Assess the morphology of the red blood cells.
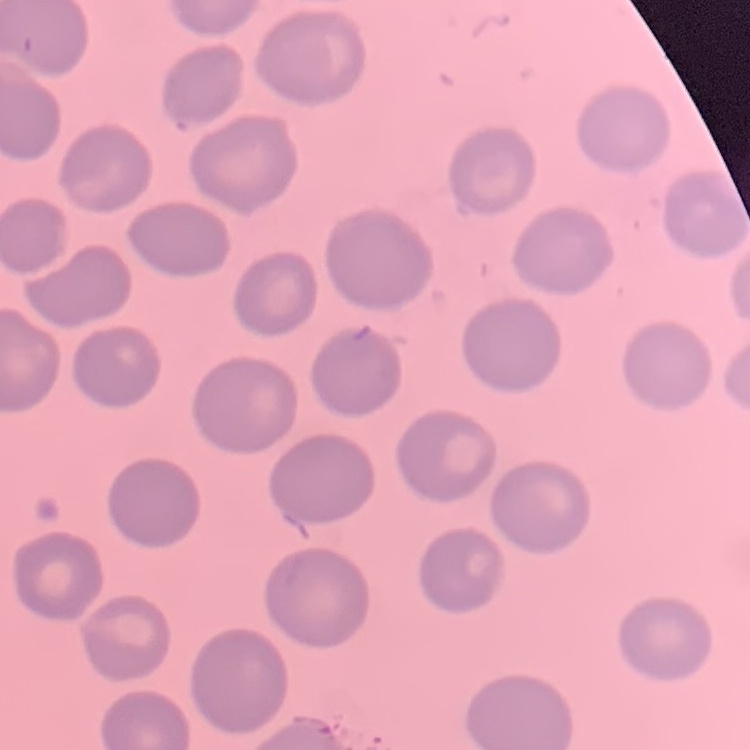
They show no rouleaux formation.

Summary:
  - Stain: Field's or Giemsa
  - Preparation: thin peripheral smear
  - Image type: square crop of a larger photomicrograph